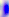

modality = photomicrograph
magnification = 400x
identification = Toxoplasma gondii